Assess this cell for malaria.
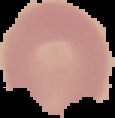

It is uninfected.

Segmented cell region on a black background. From a thin blood smear. Image is 115×118 pixels.